Assess this cell for malaria.
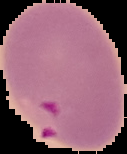

It is parasitized.

preparation: thin blood film
image_size: 127×154 pixels
image_type: segmented cell region on a black background